Report the malaria status.
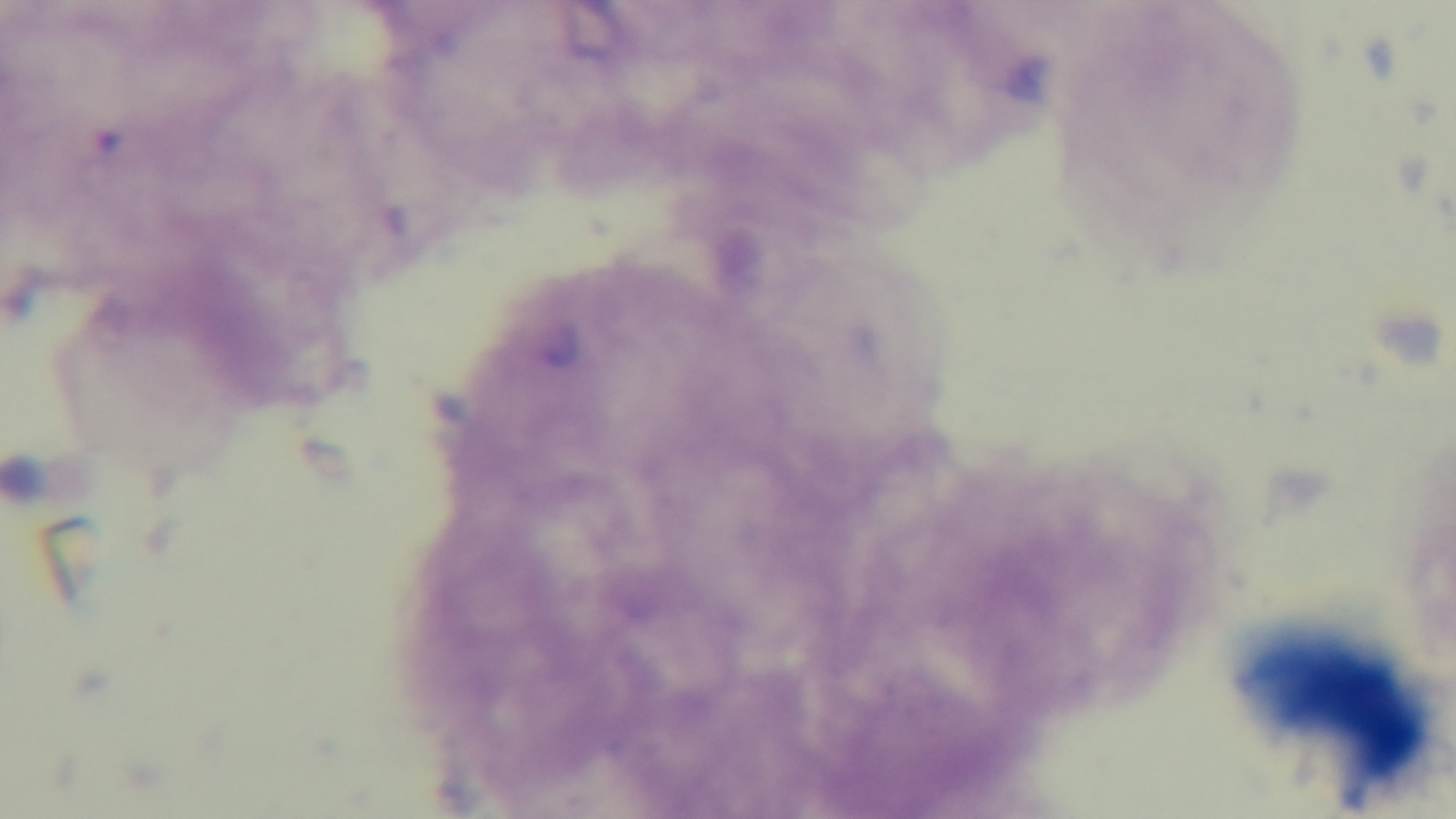
Negative.

Oil-immersion objective, 100x. Single field of view. Light microscopy. Mounted 4K digital camera. Giemsa-stained. Preparation: thick.